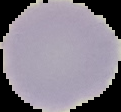
Summary:
  - Image type: segmented cell region with the area outside set to black
  - Preparation: thin blood smear
  - Malaria status: uninfected
  - Image size: 121×112 pixels